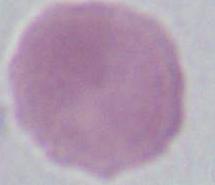 Photomicrograph. An erythrocyte is seen. Captured at 1000x magnification.